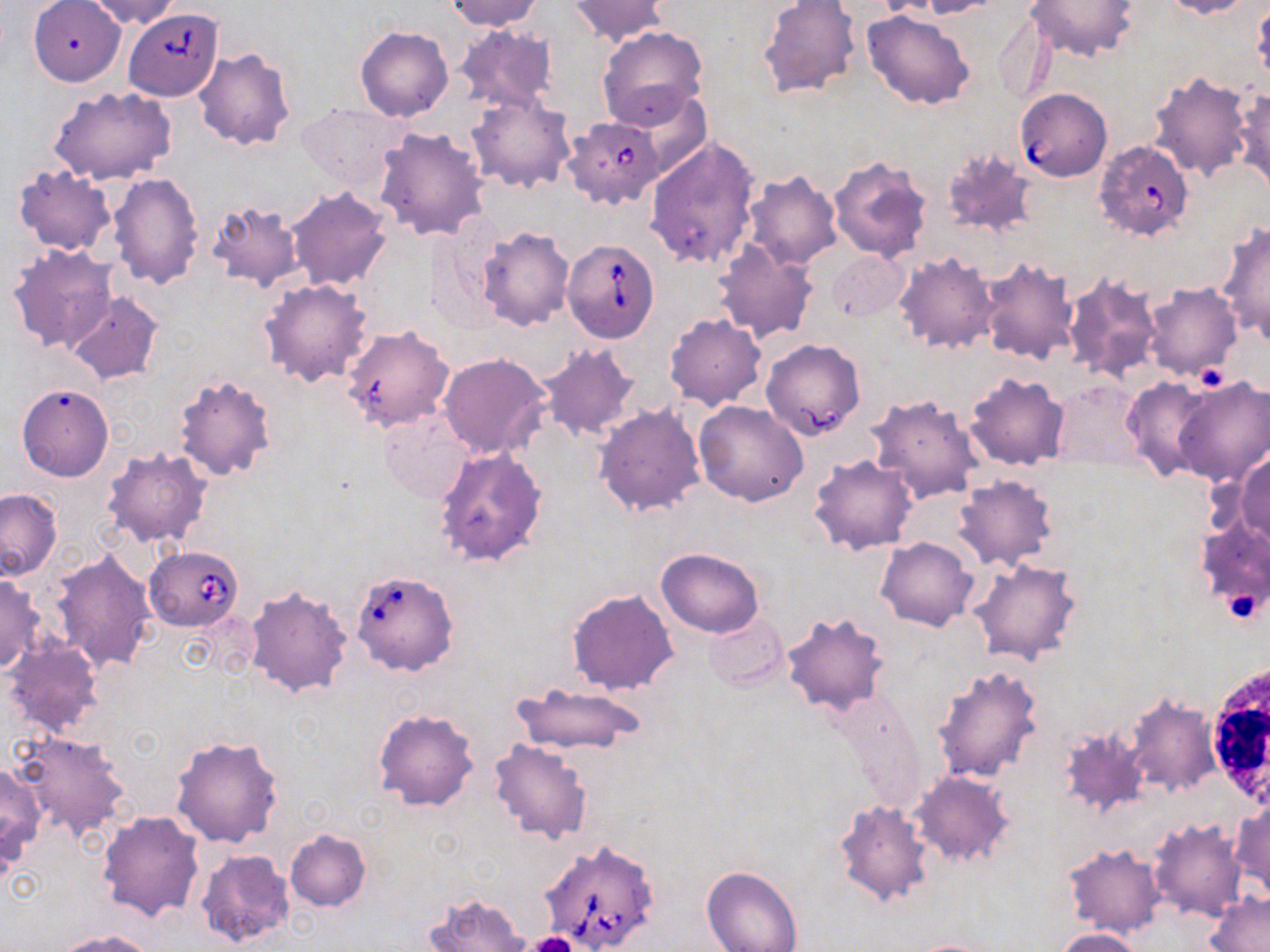
slide-level diagnosis = Babesia divergens
stain = May-Grünwald-Giemsa
uninfected red blood cell locations = approximate bounding boxes as (x1, y1, x2, y2) in pixels: (82, 0, 186, 27), (445, 0, 544, 31), (568, 0, 670, 46), (757, 0, 862, 100), (916, 0, 1001, 18), (1025, 0, 1139, 61), (1158, 0, 1255, 18), (1250, 1, 1269, 85), (28, 3, 126, 86), (862, 9, 975, 110), (993, 10, 1054, 105), (452, 24, 560, 119), (355, 26, 453, 122), (597, 26, 709, 129), (192, 48, 296, 151), (1147, 71, 1253, 180), (614, 84, 716, 181), (49, 86, 177, 185), (1232, 88, 1270, 196), (465, 91, 576, 194), (296, 102, 410, 198), (374, 127, 492, 241), (644, 136, 760, 272), (940, 147, 1038, 241), (828, 153, 935, 261), (13, 164, 118, 257), (741, 170, 842, 271), (109, 171, 203, 290), (287, 187, 393, 292), (206, 201, 305, 295), (1216, 221, 1270, 345), (425, 222, 506, 330), (477, 227, 575, 331), (713, 239, 819, 344), (7, 244, 118, 353), (828, 250, 909, 322), (894, 251, 999, 355), (976, 256, 1079, 364), (1062, 273, 1162, 383), (259, 278, 374, 388), (1144, 283, 1243, 382), (65, 290, 164, 385), (664, 312, 766, 411), (340, 324, 455, 432), (761, 338, 865, 440), (536, 341, 640, 442), (439, 353, 552, 459), (965, 372, 1069, 469), (174, 373, 277, 482), (1172, 374, 1270, 486), (1122, 376, 1214, 481), (1051, 381, 1144, 468), (16, 384, 114, 481), (867, 393, 985, 505), (694, 402, 809, 506), (593, 403, 706, 518), (379, 411, 477, 504), (434, 445, 549, 567), (101, 446, 212, 549), (1234, 451, 1270, 546), (809, 453, 918, 554), (953, 475, 1057, 572), (0, 488, 63, 580), (1193, 516, 1270, 623), (877, 536, 978, 631), (656, 547, 763, 637), (50, 548, 159, 674), (970, 558, 1082, 666), (0, 573, 45, 674), (243, 585, 354, 699), (567, 587, 680, 696), (781, 612, 889, 715), (705, 613, 788, 691), (2, 639, 104, 738), (932, 663, 1045, 783), (510, 681, 647, 758), (1122, 692, 1220, 796), (373, 708, 478, 811), (1058, 725, 1148, 818), (10, 729, 132, 841), (170, 734, 284, 847), (489, 739, 592, 845), (0, 762, 48, 865), (908, 770, 1013, 867), (1232, 800, 1269, 897), (835, 801, 932, 907), (98, 810, 204, 921), (1148, 816, 1248, 921), (285, 828, 372, 913), (1063, 842, 1166, 939), (196, 848, 297, 950), (702, 865, 805, 952), (424, 892, 532, 952), (1205, 892, 1270, 952), (1056, 928, 1142, 952), (55, 930, 155, 952), (906, 939, 1000, 952)
platelet locations = approximate bounding boxes as (x1, y1, x2, y2) in pixels: (1197, 360, 1226, 394), (1223, 585, 1265, 625), (524, 932, 580, 952)
magnification = 1000x
image size = 1270×952 pixels
preparation = thin blood smear
modality = light microscopy
field of view = single
white blood cell locations = approximate bounding boxes as (x1, y1, x2, y2) in pixels: (1211, 663, 1270, 813)
Babesia divergens-infected red blood cell locations = approximate bounding boxes as (x1, y1, x2, y2) in pixels: (127, 12, 224, 104), (1012, 88, 1110, 184), (563, 117, 664, 210), (1094, 139, 1194, 241), (562, 239, 660, 342), (144, 545, 245, 630), (349, 570, 459, 677), (536, 839, 660, 952)